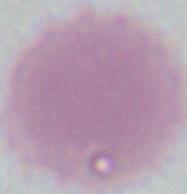
Summary:
  - Magnification: 1000x
  - Modality: micrograph
  - Identification: erythrocyte